Outline every Plasmodium parasite, every leukocyte, and every artifact (stain precipitate or debris).
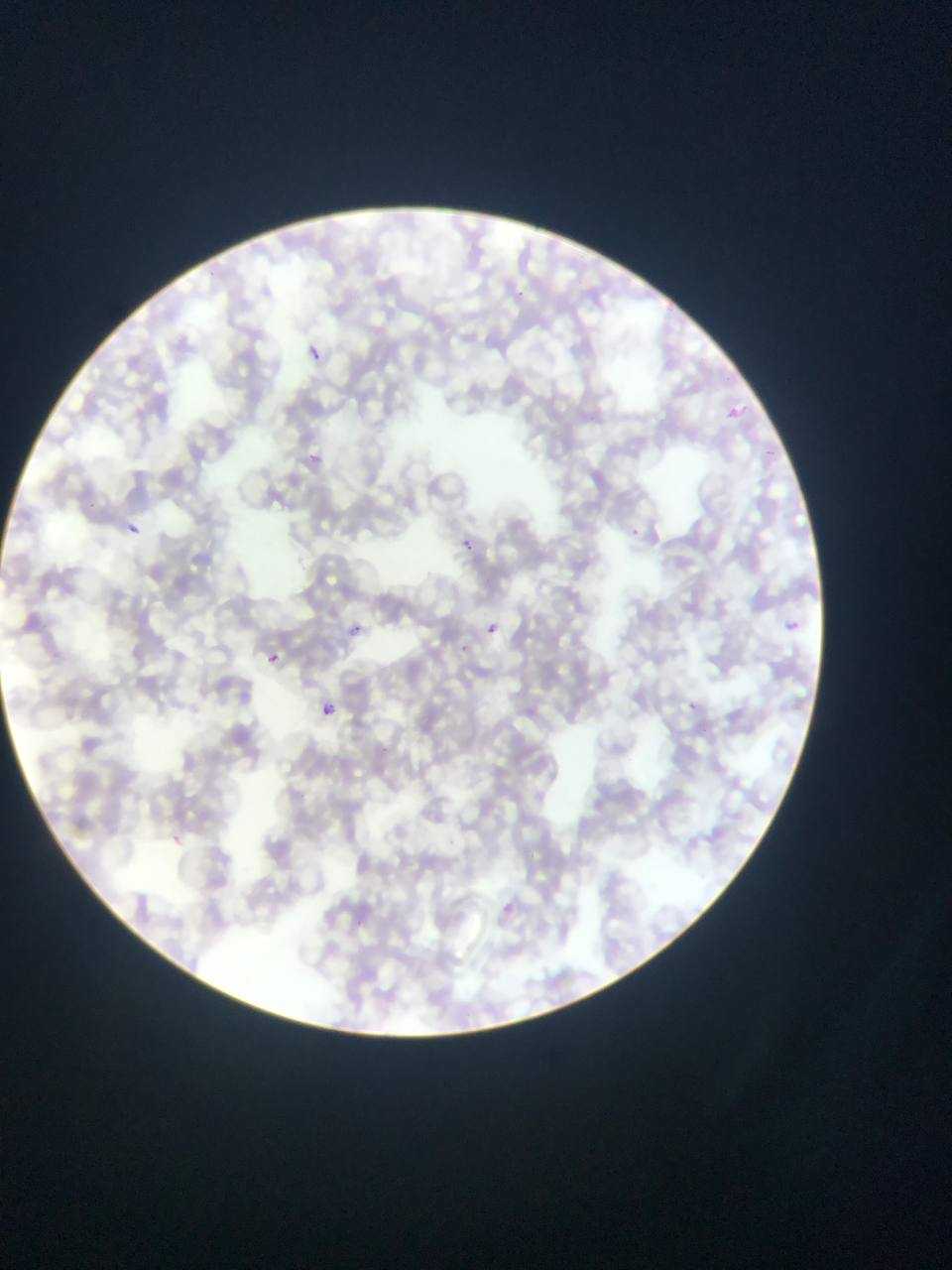

Approximate bounding boxes as [left, top, right, bottom] in pixels.
Plasmodium parasites: [306, 343, 322, 361], [717, 402, 760, 428], [307, 450, 323, 465], [125, 522, 140, 537], [455, 526, 485, 559], [489, 612, 509, 643], [780, 612, 820, 647], [347, 614, 370, 645], [264, 637, 307, 668], [459, 637, 476, 688], [322, 703, 334, 715].
No leukocytes observed.

capture = mobile-phone photograph through a microscope
country = Ghana
image size = 952×1270 pixels
preparation = thin blood film
field of view = single